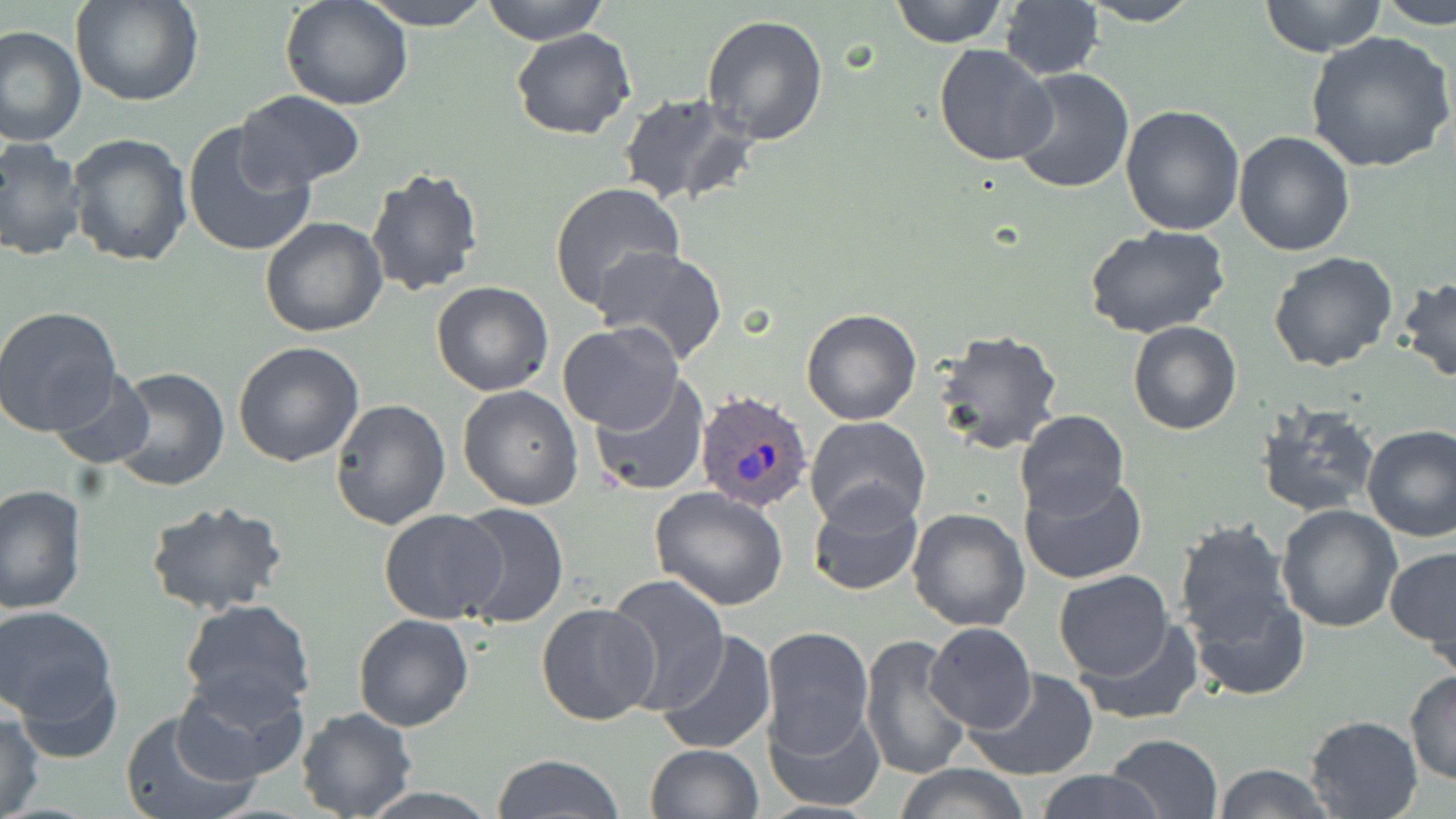

slide_level_diagnosis: Plasmodium ovale
modality: light microscopy
plasmodium_ovale_infected_red_blood_cell_locations: 'approximate bounding boxes as (x1, y1, x2, y2) in pixels: (695, 392, 814, 515)'
uninfected_red_blood_cell_locations: 'approximate bounding boxes as (x1, y1, x2, y2) in pixels: (69, 0, 205, 108), (282, 0, 413, 110), (361, 0, 497, 29), (481, 0, 612, 43), (891, 0, 1007, 46), (1260, 0, 1384, 57), (1378, 0, 1455, 25), (1077, 2, 1202, 26), (998, 3, 1104, 81), (700, 14, 829, 146), (2, 25, 86, 146), (511, 28, 637, 141), (1303, 31, 1456, 176), (933, 44, 1058, 166), (1009, 67, 1136, 195), (613, 91, 756, 209), (235, 92, 366, 191), (1120, 103, 1248, 234), (182, 122, 316, 259), (1234, 130, 1355, 256), (67, 131, 194, 268), (0, 139, 88, 263), (364, 166, 485, 298), (548, 181, 686, 312), (258, 217, 387, 337), (1083, 224, 1231, 339), (593, 247, 729, 368), (1268, 251, 1401, 373), (1397, 276, 1456, 384), (431, 281, 553, 396), (0, 306, 125, 438), (800, 308, 923, 425), (1127, 319, 1243, 436), (558, 323, 684, 433), (933, 328, 1064, 456), (233, 341, 364, 467), (107, 366, 229, 492), (46, 369, 154, 472), (587, 373, 710, 498), (457, 385, 584, 511), (330, 399, 452, 532), (1255, 401, 1379, 518), (1015, 409, 1129, 517), (805, 416, 931, 529), (1362, 425, 1456, 543), (1018, 471, 1148, 586), (0, 485, 86, 613), (808, 485, 924, 598), (648, 486, 790, 610), (144, 500, 291, 618), (1276, 504, 1403, 631), (452, 505, 569, 627), (906, 508, 1030, 632), (379, 511, 509, 625), (1173, 520, 1296, 649), (1383, 548, 1456, 654), (1051, 569, 1175, 681), (605, 574, 730, 709), (1188, 588, 1309, 700), (178, 599, 318, 716), (536, 602, 660, 725), (1, 605, 118, 726), (353, 613, 474, 731), (1074, 619, 1202, 726), (922, 622, 1036, 735), (759, 627, 875, 759), (657, 630, 777, 755), (857, 634, 973, 782), (8, 651, 122, 767), (172, 668, 311, 785), (965, 668, 1100, 781), (1404, 670, 1456, 786), (765, 700, 887, 810), (295, 707, 418, 819), (0, 709, 44, 819), (118, 709, 256, 819), (1305, 715, 1424, 819), (1106, 733, 1222, 819), (643, 743, 763, 819), (492, 754, 625, 819), (893, 763, 1030, 819), (1213, 763, 1334, 819), (1033, 769, 1165, 819), (356, 785, 500, 817)'
magnification: 1000x
field_of_view: one of a larger specimen
stain: May-Grünwald-Giemsa
image_size: 1456×819 pixels
preparation: thin blood smear